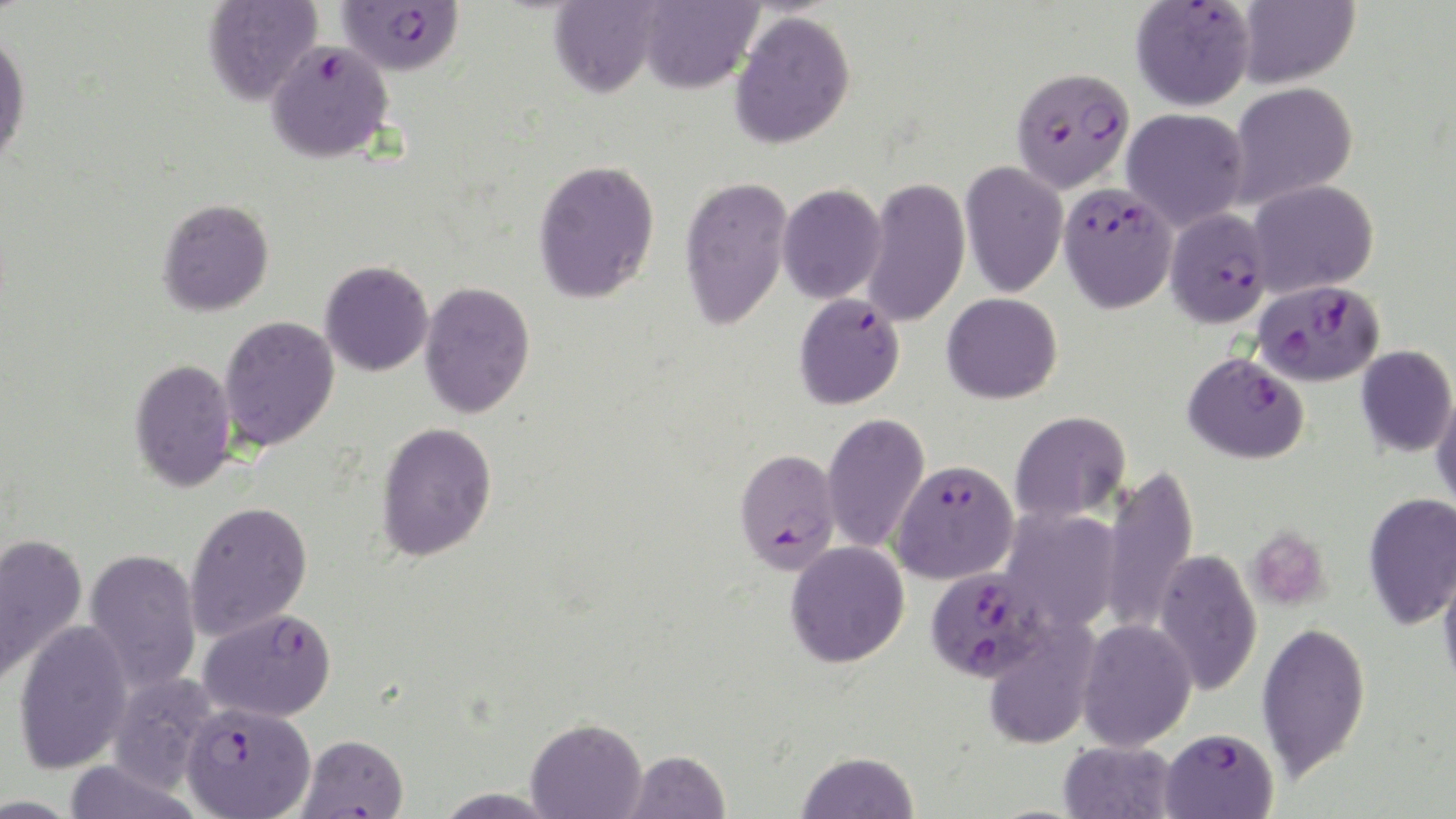

Approximate bounding boxes as (x1, y1, x2, y2) in pixels. Uninfected red blood cell locations (subset): (202, 0, 322, 105), (549, 0, 663, 97), (1237, 0, 1360, 88), (637, 1, 762, 94), (729, 10, 856, 150), (0, 29, 31, 168), (1228, 82, 1358, 208), (1122, 108, 1249, 231), (533, 159, 661, 304), (960, 161, 1067, 298), (679, 175, 793, 331), (862, 178, 970, 328), (1248, 180, 1378, 297), (777, 183, 888, 304), (157, 198, 275, 316), (320, 260, 434, 376), (419, 280, 536, 418), (942, 292, 1062, 404), (219, 315, 340, 451), (1356, 345, 1456, 457), (1184, 351, 1310, 463), (129, 357, 237, 492), (1431, 388, 1456, 515), (1010, 410, 1131, 524), (822, 412, 930, 554), (375, 420, 498, 562), (1100, 463, 1199, 637), (1363, 492, 1456, 630), (184, 500, 313, 640), (1000, 508, 1121, 632), (0, 533, 88, 685), (785, 541, 910, 668), (83, 548, 202, 694), (1152, 548, 1262, 696), (1438, 559, 1456, 695), (982, 617, 1100, 750), (13, 619, 134, 774), (1075, 619, 1197, 751), (1256, 620, 1371, 782), (106, 673, 219, 792), (526, 717, 646, 818), (1058, 740, 1178, 819), (624, 749, 730, 819), (796, 750, 918, 818), (63, 760, 201, 819), (432, 787, 561, 818). Platelet locations: (1245, 527, 1331, 612). Plasmodium falciparum-infected red blood cell locations (subset): (1131, 1, 1256, 112), (265, 40, 394, 164), (1011, 66, 1135, 193), (1058, 183, 1178, 313), (1165, 208, 1272, 328), (1254, 280, 1384, 386), (793, 292, 905, 409), (734, 448, 841, 574), (890, 459, 1019, 584), (923, 566, 1052, 682), (198, 608, 337, 723), (181, 702, 316, 819), (1160, 726, 1278, 818), (297, 734, 409, 819). Slide-level diagnosis: Plasmodium falciparum. Light microscopy. One field of a larger specimen. Thin blood film. 1000x magnification. Image is 1456×819 pixels. May-Grünwald-Giemsa-stained preparation.